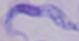
Summary:
  - Modality: photomicrograph
  - Magnification: 1000x
  - Identification: trypanosome